Give the extent of all uninfected red blood cells.
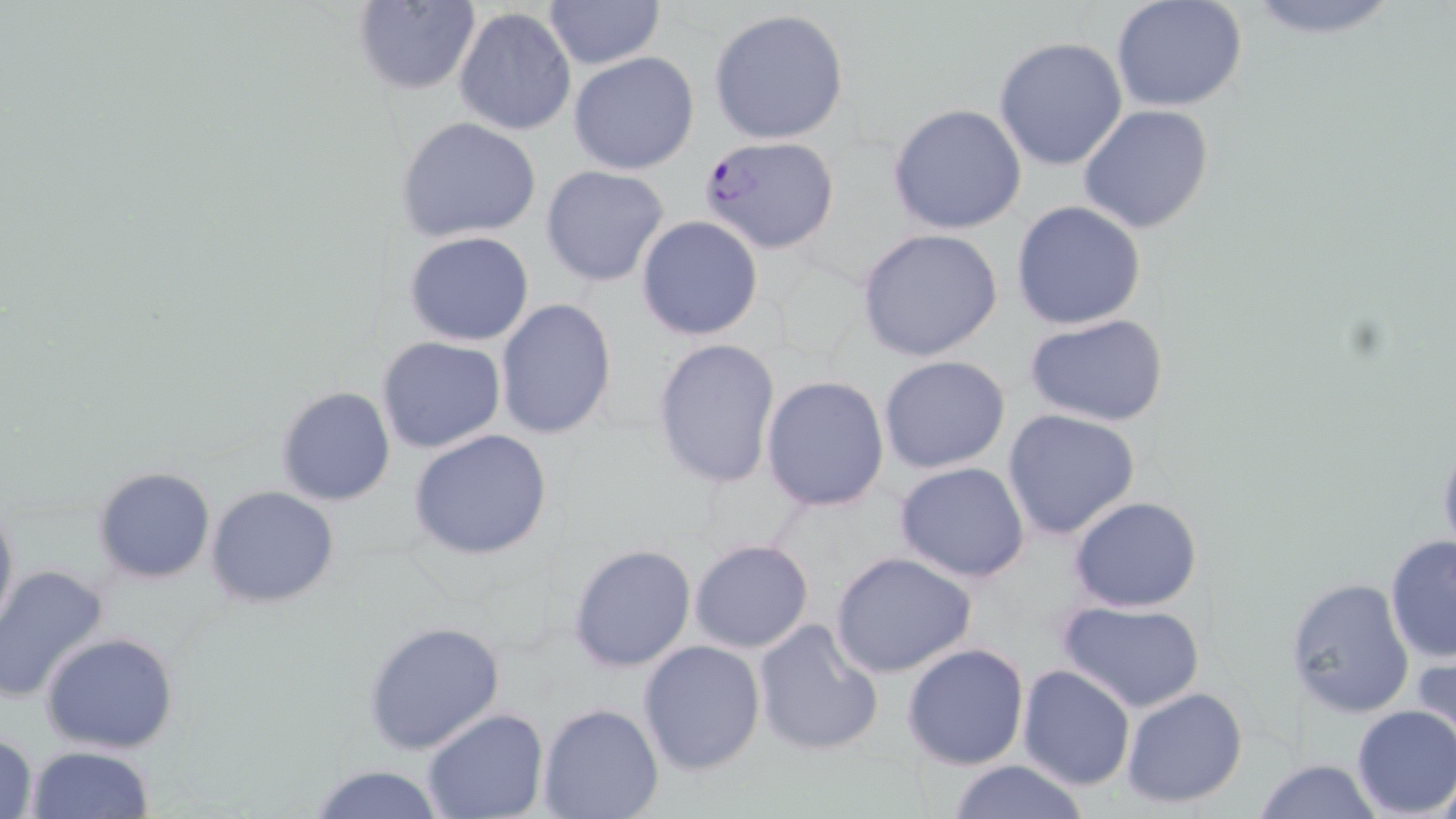
Approximate bounding boxes as (x1, y1, x2, y2) in pixels.
Uninfected red blood cells: (543, 0, 667, 69), (1237, 0, 1410, 41), (350, 1, 482, 96), (1112, 2, 1248, 113), (453, 6, 578, 137), (708, 8, 851, 146), (992, 36, 1128, 172), (568, 51, 700, 174), (887, 103, 1028, 233), (1079, 104, 1214, 234), (395, 117, 544, 244), (541, 164, 670, 287), (1010, 200, 1146, 330), (635, 217, 764, 340), (855, 228, 1004, 361), (404, 231, 536, 347), (494, 297, 619, 439), (1026, 312, 1170, 427), (376, 336, 506, 455), (650, 337, 782, 491), (879, 354, 1012, 475), (761, 375, 890, 511), (276, 386, 398, 506), (1002, 408, 1142, 541), (407, 428, 555, 561), (894, 460, 1031, 582), (93, 465, 217, 584), (206, 485, 341, 608), (0, 492, 18, 640), (1068, 495, 1205, 611), (1384, 533, 1456, 666), (687, 539, 814, 653), (568, 542, 696, 672), (830, 551, 978, 679), (0, 566, 112, 704), (1285, 576, 1416, 719), (1059, 600, 1205, 714), (363, 619, 507, 757), (751, 619, 884, 758), (41, 633, 181, 755), (637, 640, 767, 778), (902, 641, 1031, 771), (1410, 649, 1455, 760), (1017, 664, 1136, 791), (1120, 685, 1249, 809), (537, 703, 664, 819), (1350, 705, 1456, 818), (422, 706, 549, 819), (1, 731, 39, 818), (24, 745, 155, 819), (1252, 758, 1384, 818), (944, 759, 1094, 819), (308, 763, 448, 819).

Plasmodium falciparum-infected red blood cell locations: (698, 134, 842, 255). Slide-level diagnosis: Plasmodium falciparum. Light microscopy. Image is 1456×819 pixels. Single field of view. Captured at 1000x magnification. May-Grünwald-Giemsa stain. Thin blood smear.